Comment on the morphology of the red blood cells.
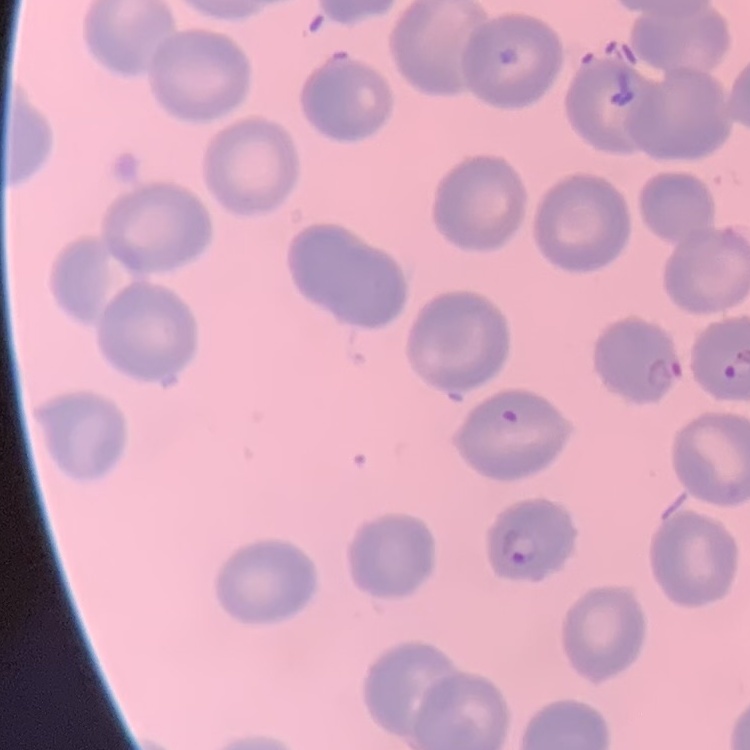

No rouleaux formation.

stain = Field's or Giemsa
image type = one tile cut from a larger photomicrograph
preparation = thin blood smear